Identify the parasite.
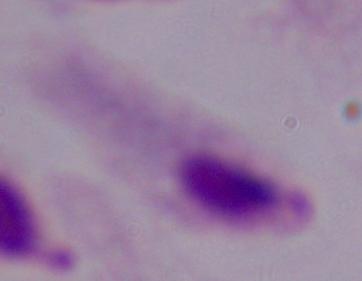

A trichomonad.

1000x magnification. Photomicrograph.